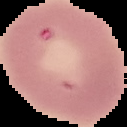
{
  "image_size": "127×127 pixels",
  "image_type": "cell region segmented out of the field of view; surrounding area masked to black",
  "malaria_status": "uninfected",
  "preparation": "thin blood smear"
}